Assess this cell for malaria.
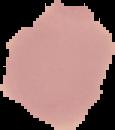
It is uninfected.

Summary:
  - Image size: 115×130 pixels
  - Image type: segmented cell region with the area outside set to black
  - Preparation: thin blood smear